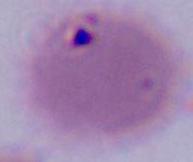 Photomicrograph. 1000x magnification. An erythrocyte is seen.